Give the preparation type.
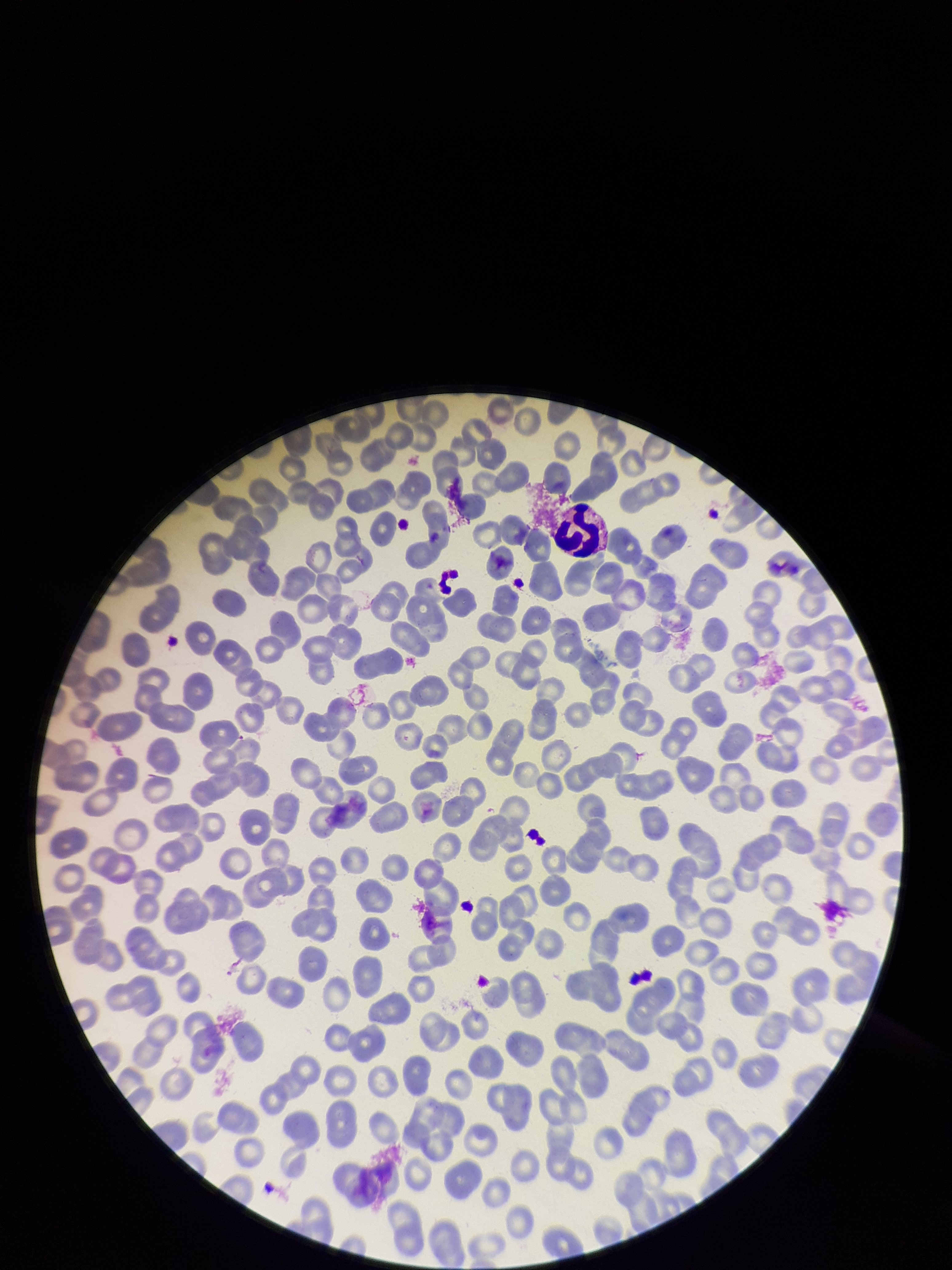

A thin smear.

Summary:
  - Stain: Giemsa
  - Parasitized red blood cell count: 0
  - Parasitized red blood cells: none identified
  - Field of view: single
  - Patient malaria status: negative
  - Image size: 952×1270 pixels
  - Capture: smartphone photograph through the microscope eyepiece
  - Red blood cell count: 265